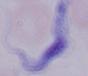

Summary:
  - Identification: trypanosome
  - Magnification: 1000x
  - Modality: photomicrograph